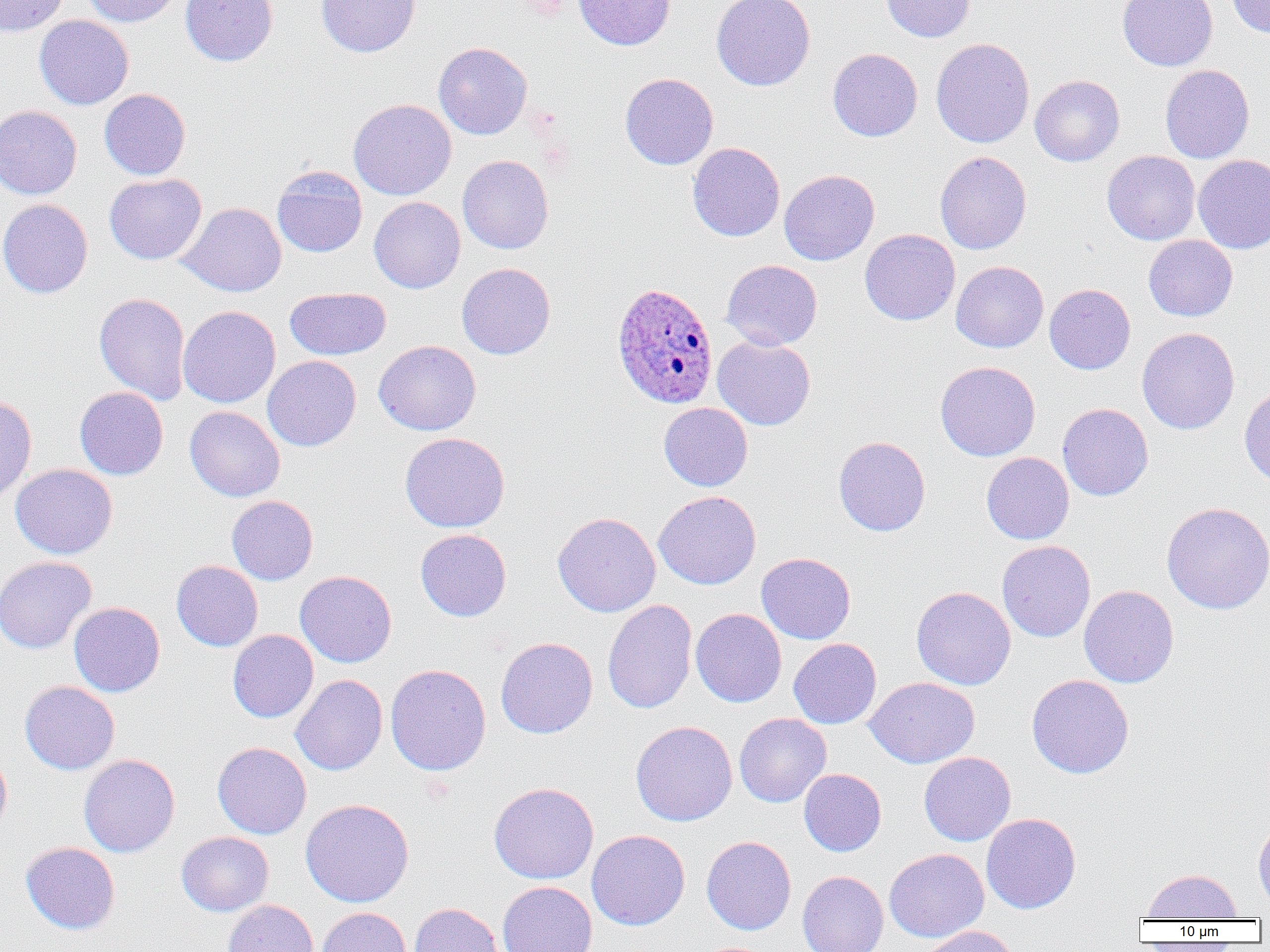

Summary:
  - Coordinate format: approximate bounding boxes as (x1,y1)-(x2,y2) corner pairs in pixels
  - Uninfected red blood cell locations: (0,0)-(69,36), (81,0)-(183,27), (180,0)-(278,66), (316,0)-(421,58), (574,0)-(675,50), (712,0)-(815,91), (881,0)-(975,42), (1117,0)-(1218,71), (1226,0)-(1270,36), (34,15)-(134,110), (931,38)-(1035,148), (434,42)-(532,139), (828,48)-(923,141), (1160,64)-(1255,164), (620,72)-(718,170), (1030,75)-(1124,167), (99,89)-(191,180), (348,98)-(456,200), (0,105)-(82,199), (687,142)-(785,241), (935,151)-(1031,254), (1102,151)-(1200,245), (457,155)-(554,254), (1193,155)-(1270,254), (272,165)-(368,257), (779,169)-(880,266), (104,173)-(207,264), (369,197)-(465,293), (0,199)-(93,298), (178,202)-(287,297), (860,229)-(960,325), (1143,235)-(1238,322), (721,260)-(822,350), (951,261)-(1048,353), (456,263)-(555,360), (1045,284)-(1136,374), (285,287)-(391,360), (93,293)-(191,404), (178,306)-(280,408), (1137,327)-(1240,434), (712,336)-(816,431), (374,340)-(481,436), (263,355)-(361,451), (935,361)-(1040,461), (1239,382)-(1270,486), (74,387)-(168,480), (0,394)-(37,504), (659,403)-(753,491), (1057,403)-(1153,501), (185,406)-(285,502), (399,432)-(510,533), (833,436)-(931,536), (981,452)-(1074,544), (10,464)-(118,559), (654,490)-(761,589), (227,495)-(318,585), (1161,501)-(1270,614), (552,512)-(661,617), (415,529)-(511,621), (997,540)-(1095,642), (756,552)-(856,644), (0,556)-(96,653), (171,560)-(263,651), (295,570)-(397,667), (1079,585)-(1179,688), (911,586)-(1016,690), (602,599)-(697,714), (69,602)-(165,697), (690,608)-(787,707), (228,630)-(319,723), (495,637)-(598,738), (788,638)-(882,728), (385,663)-(491,776), (291,674)-(388,775), (1026,674)-(1134,779), (864,677)-(979,768), (20,681)-(120,774), (734,713)-(831,807), (630,721)-(738,826), (212,742)-(312,839), (0,748)-(12,838), (918,752)-(1015,846), (79,754)-(180,857), (799,768)-(886,856), (488,782)-(599,884), (300,798)-(414,907), (980,812)-(1081,914), (1253,818)-(1270,911), (586,830)-(690,930), (176,832)-(274,916), (701,836)-(796,935), (21,842)-(120,935), (884,848)-(989,942), (1141,868)-(1242,920), (797,871)-(888,952), (497,881)-(597,952), (223,899)-(318,952), (408,902)-(506,952), (316,906)-(411,952), (919,925)-(1022,952)
  - Plasmodium ovale-infected red blood cell locations: (612,282)-(718,408)
  - Slide-level diagnosis: Plasmodium ovale
  - Preparation: thin blood film
  - Modality: optical microscopy
  - Magnification: 1000x
  - Image size: 1270×952 pixels
  - Field of view: one of a larger specimen